Name the cell type shown.
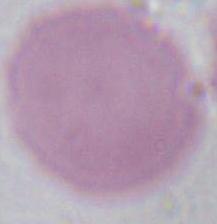
An erythrocyte.

Captured at 1000x magnification. Photomicrograph.